Assess this cell for malaria.
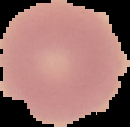

It is uninfected.

The area outside the segmented cell region is set to black. From a thin blood smear. Image is 130×127 pixels.